Locate platelets.
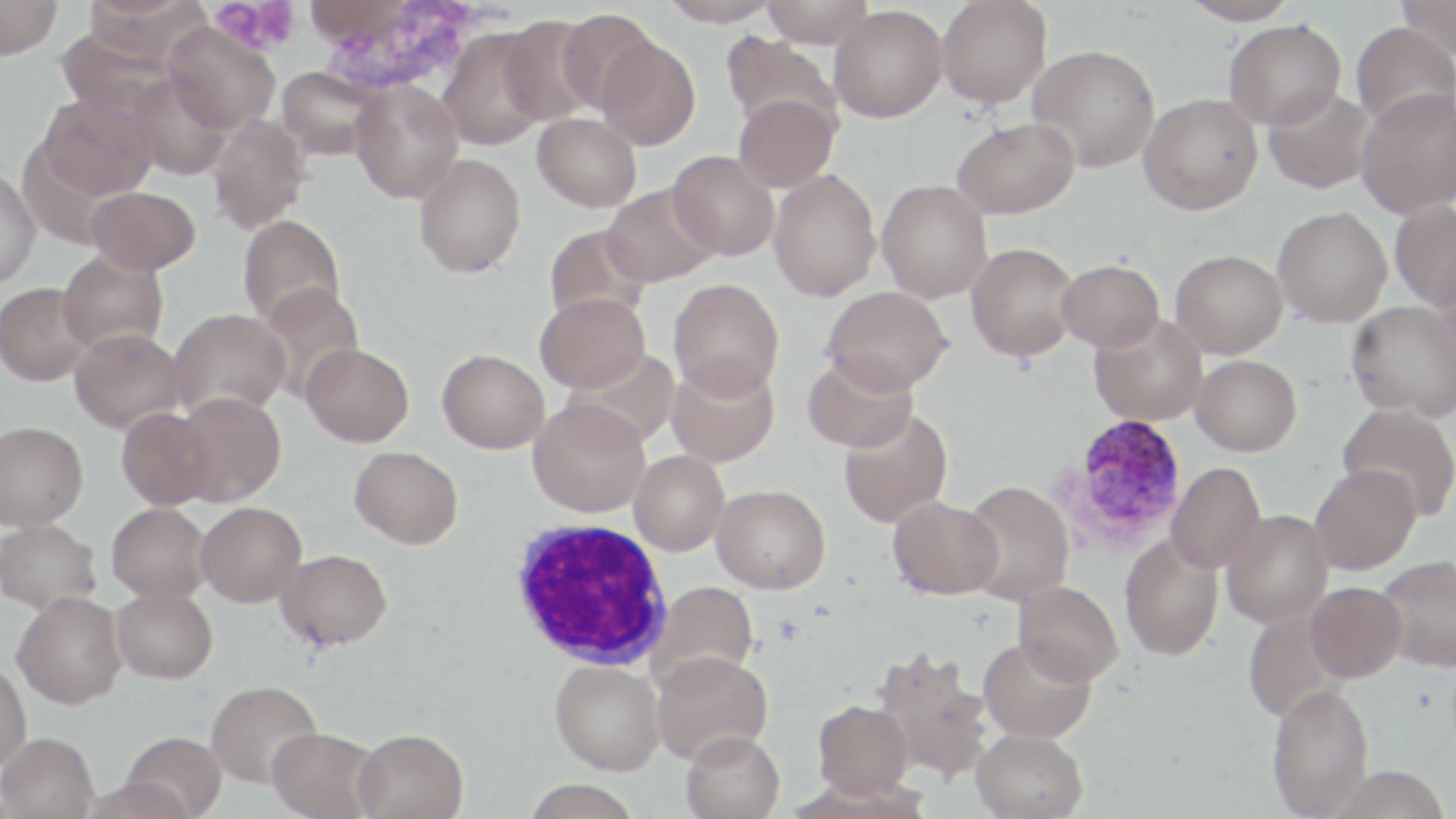
Approximate bounding boxes as [x1, y1, x2, y2] in pixels.
Platelets: [209, 0, 300, 56].

slide-level diagnosis = Plasmodium vivax
magnification = 1000x
preparation = thin blood film
modality = light microscopy
Plasmodium vivax-infected red blood cell locations = approximate bounding boxes as [x1, y1, x2, y2] in pixels: [1058, 414, 1189, 551]
field of view = one of a larger specimen
white blood cell locations = approximate bounding boxes as [x1, y1, x2, y2] in pixels: [508, 519, 672, 669]
uninfected red blood cell locations = approximate bounding boxes as [x1, y1, x2, y2] in pixels: [0, 0, 63, 60], [660, 0, 782, 27], [761, 0, 875, 48], [937, 0, 1052, 109], [1178, 0, 1298, 26], [1395, 0, 1456, 61], [829, 6, 947, 122], [555, 10, 660, 114], [498, 16, 603, 126], [1223, 19, 1346, 130], [163, 22, 280, 133], [1350, 22, 1455, 132], [438, 29, 551, 151], [721, 33, 840, 135], [596, 37, 701, 150], [1027, 45, 1159, 173], [277, 66, 385, 161], [129, 75, 232, 180], [350, 81, 464, 204], [1263, 87, 1375, 194], [1356, 87, 1456, 219], [1138, 93, 1262, 215], [38, 94, 156, 200], [733, 94, 839, 193], [532, 113, 641, 212], [207, 115, 312, 235], [952, 117, 1080, 219], [667, 150, 780, 260], [413, 153, 526, 278], [768, 169, 881, 301], [0, 170, 41, 288], [876, 179, 992, 303], [601, 184, 720, 287], [86, 186, 200, 274], [1389, 200, 1456, 310], [1272, 206, 1392, 327], [237, 215, 347, 329], [544, 224, 652, 327], [966, 242, 1081, 362], [1170, 249, 1287, 358], [58, 250, 169, 354], [1429, 257, 1456, 371], [1057, 259, 1163, 351], [668, 278, 784, 401], [0, 282, 95, 386], [256, 282, 364, 400], [821, 287, 953, 395], [535, 293, 649, 393], [1346, 300, 1456, 421], [169, 307, 291, 420], [1090, 312, 1208, 426], [69, 327, 186, 433], [301, 342, 413, 446], [437, 348, 550, 453], [566, 348, 681, 450], [1191, 354, 1302, 457], [803, 355, 918, 453], [666, 358, 780, 468], [173, 392, 286, 506], [527, 399, 650, 518], [1337, 402, 1456, 521], [116, 407, 218, 510], [838, 408, 953, 528], [0, 421, 89, 530], [350, 445, 463, 548], [629, 450, 730, 555], [1167, 462, 1266, 573], [1309, 464, 1421, 575], [961, 479, 1074, 604], [711, 484, 830, 594], [887, 496, 1003, 600], [196, 502, 306, 607], [106, 503, 211, 603], [1220, 509, 1333, 628], [0, 519, 101, 615], [1119, 535, 1224, 661], [275, 549, 392, 651], [1376, 554, 1456, 672], [1014, 580, 1123, 685], [648, 581, 759, 687], [1305, 581, 1407, 683], [111, 589, 217, 687], [11, 594, 127, 713], [978, 636, 1096, 743], [872, 649, 992, 784], [651, 651, 773, 765], [550, 659, 665, 775], [0, 664, 32, 774], [206, 681, 323, 791], [1267, 683, 1375, 817], [813, 699, 914, 799], [971, 728, 1088, 819], [267, 729, 380, 819], [682, 729, 785, 819], [352, 730, 469, 819], [122, 735, 225, 819], [0, 736, 99, 819], [522, 779, 643, 819], [80, 780, 194, 819]
image size = 1456×819 pixels
stain = May-Grünwald-Giemsa